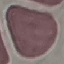 Result: no malaria parasites detected. Acquired by smartphone through the microscope eyepiece. Giemsa-stained preparation. Automatically extracted cell patch, resized to 64 × 64 pixels. Thin smear of blood.